Describe the morphology of the red blood cells.
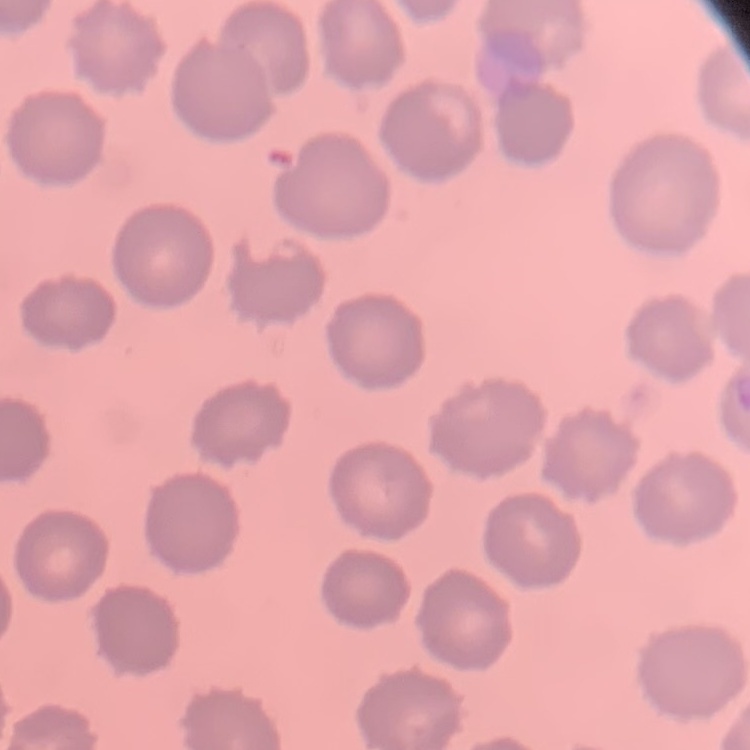

They show no rouleaux formation.

Square crop of a larger photomicrograph. Thin blood film. Stained with either Field's or Giemsa.